Identify the parasite.
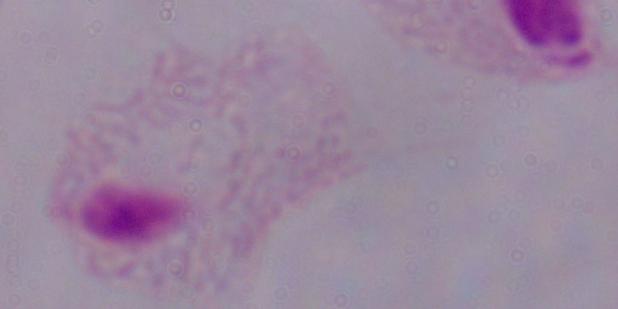
This is a trichomonad.

Captured at 1000x magnification. Micrograph.